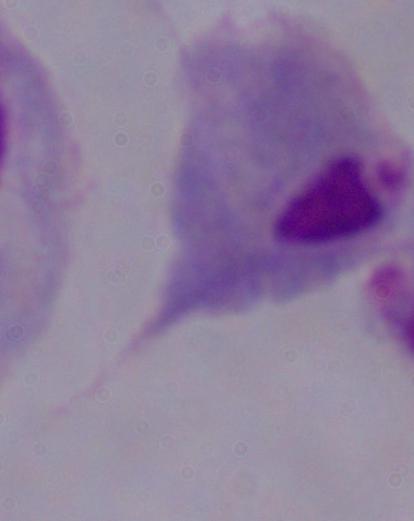 A trichomonad is seen. Photomicrograph. 1000x magnification.